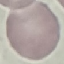
malaria status = uninfected
stain = Giemsa
image type = cell patch, automatically extracted from a larger field of view and resized to 64 × 64 pixels
capture = smartphone through the microscope eyepiece
preparation = thin blood smear